Locate and identify every blood parasite.
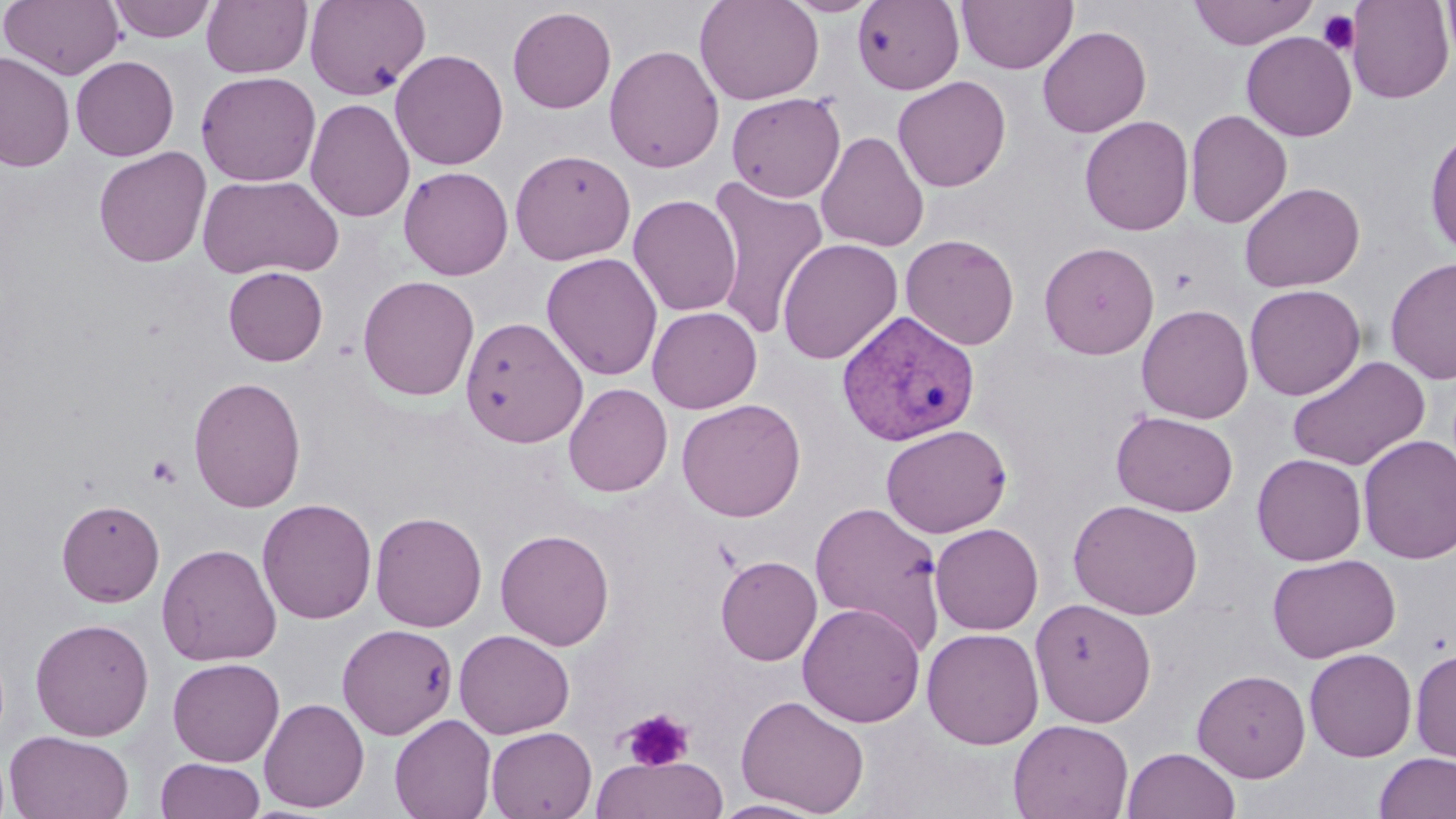
Approximate bounding boxes as [x1, y1, x2, y2] in pixels.
Plasmodium vivax-infected red blood cells: [836, 310, 981, 448].
No Plasmodium falciparum, Plasmodium ovale, Plasmodium malariae, Babesia divergens, or Trypanosoma brucei observed.

Summary:
  - Platelet locations: [1318, 9, 1360, 55], [146, 454, 182, 488], [621, 708, 693, 771]
  - Uninfected red blood cell locations: [1, 0, 125, 80], [107, 0, 217, 43], [201, 0, 313, 78], [304, 0, 431, 100], [694, 0, 824, 105], [783, 0, 881, 17], [957, 0, 1078, 74], [1188, 0, 1318, 49], [1345, 0, 1453, 103], [1442, 0, 1456, 66], [852, 1, 964, 94], [507, 6, 616, 113], [1038, 25, 1151, 138], [1241, 31, 1357, 142], [604, 44, 725, 174], [390, 49, 508, 170], [0, 50, 75, 172], [71, 55, 179, 161], [196, 71, 321, 187], [892, 75, 1011, 192], [726, 92, 846, 202], [305, 98, 414, 223], [1185, 109, 1292, 228], [1079, 115, 1194, 236], [1425, 126, 1456, 257], [816, 130, 929, 253], [93, 146, 212, 268], [510, 149, 636, 265], [398, 166, 514, 280], [197, 174, 344, 280], [706, 175, 829, 340], [1239, 182, 1365, 292], [628, 194, 741, 317], [900, 234, 1020, 350], [777, 238, 903, 365], [1038, 241, 1159, 360], [541, 252, 663, 380], [1385, 257, 1456, 384], [223, 266, 329, 366], [357, 275, 479, 401], [1244, 284, 1366, 400], [1136, 304, 1254, 424], [647, 306, 762, 413], [461, 317, 588, 447], [1287, 355, 1431, 471], [188, 376, 306, 512], [563, 382, 673, 497], [676, 398, 806, 522], [1111, 411, 1238, 516], [880, 424, 1012, 538], [1357, 435, 1456, 565], [1251, 453, 1367, 566], [257, 498, 377, 624], [56, 499, 165, 607], [1068, 499, 1203, 619], [808, 500, 945, 650], [370, 511, 487, 632], [929, 523, 1044, 635], [495, 528, 615, 651], [156, 543, 282, 667], [1267, 553, 1401, 663], [715, 555, 822, 665], [1030, 598, 1157, 726], [797, 602, 926, 727], [30, 617, 155, 741], [337, 623, 457, 740], [921, 627, 1044, 748], [454, 629, 575, 739], [1304, 648, 1417, 762], [1411, 648, 1456, 763], [167, 658, 284, 766], [1192, 668, 1311, 782], [736, 694, 869, 816], [259, 698, 369, 812], [389, 714, 496, 819], [1008, 718, 1134, 819], [485, 726, 597, 818], [4, 730, 135, 819], [1122, 747, 1240, 819], [1374, 752, 1456, 818], [592, 754, 728, 819], [154, 757, 267, 818], [710, 799, 828, 818]
  - Slide-level diagnosis: Plasmodium vivax
  - Modality: optical microscopy
  - Stain: May-Grünwald-Giemsa
  - Preparation: thin blood smear
  - Image size: 1456×819 pixels
  - Field of view: one of a larger specimen
  - Magnification: 1000x